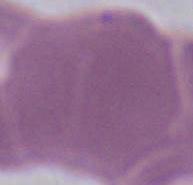

modality = photomicrograph
magnification = 1000x
identification = erythrocyte